Classify this cell by malaria status.
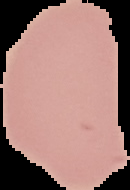

Uninfected.

Summary:
  - Image type: segmented cell region on a black background
  - Image size: 130×190 pixels
  - Preparation: thin blood film